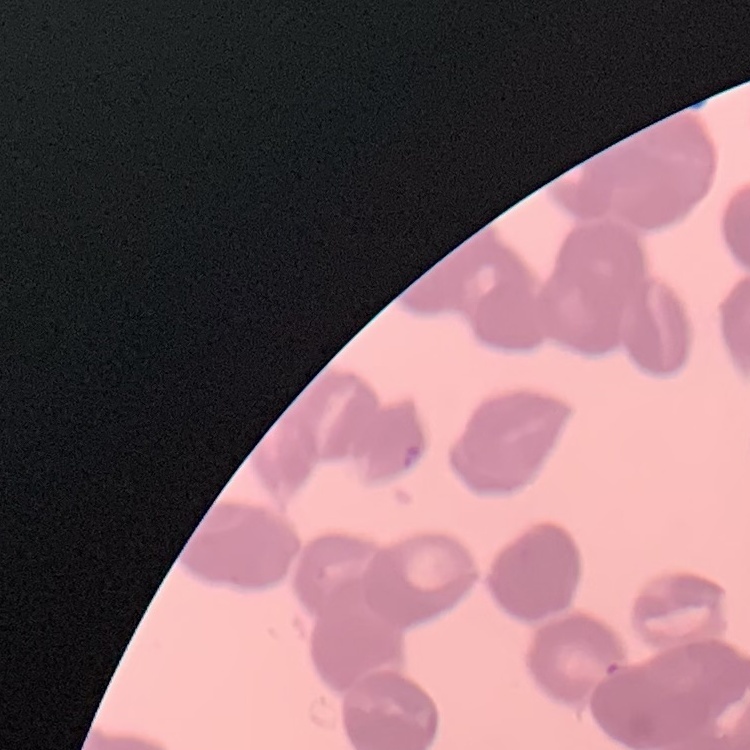
Summary:
  - Erythrocyte morphology: rouleaux formation
  - Preparation: thin blood smear
  - Image type: square crop of a larger photomicrograph
  - Stain: Field's or Giemsa